Locate every blood parasite and identify its species.
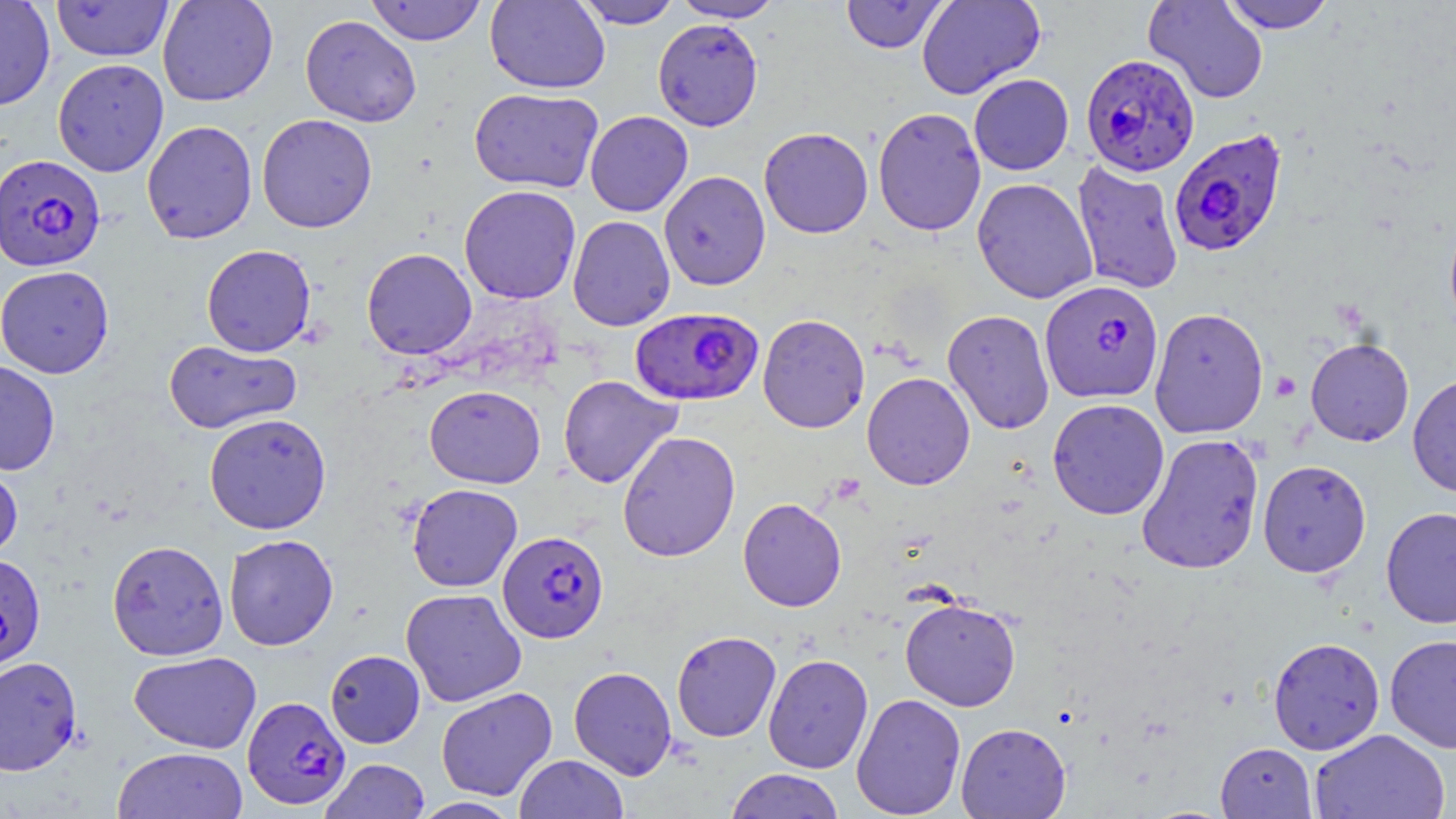
Approximate bounding boxes as [x1, y1, x2, y2] in pixels.
Plasmodium falciparum-infected red blood cells: [1080, 53, 1199, 176], [1168, 127, 1289, 257], [0, 154, 105, 271], [1040, 279, 1164, 404], [630, 306, 763, 407], [497, 530, 608, 643], [0, 553, 46, 671], [242, 695, 351, 810].
No Plasmodium ovale, Plasmodium malariae, Plasmodium vivax, Babesia divergens, or Trypanosoma brucei observed.

Uninfected red blood cell locations: [0, 0, 55, 110], [157, 0, 278, 106], [365, 0, 487, 46], [486, 0, 610, 94], [573, 0, 682, 29], [670, 0, 785, 22], [840, 0, 949, 54], [916, 0, 1045, 99], [1143, 0, 1269, 104], [1220, 0, 1335, 33], [51, 1, 174, 62], [300, 14, 422, 127], [652, 18, 763, 131], [53, 59, 169, 175], [969, 74, 1074, 175], [469, 87, 604, 194], [873, 106, 986, 236], [585, 111, 693, 217], [256, 114, 378, 233], [141, 120, 258, 244], [759, 127, 874, 238], [1071, 160, 1184, 295], [658, 170, 771, 291], [972, 177, 1098, 304], [459, 185, 582, 304], [1443, 208, 1456, 341], [567, 215, 675, 331], [201, 244, 316, 356], [361, 248, 477, 359], [0, 265, 114, 378], [1149, 307, 1269, 439], [942, 309, 1055, 434], [757, 313, 870, 433], [1305, 337, 1414, 446], [163, 339, 302, 434], [0, 360, 61, 476], [862, 371, 975, 490], [1407, 372, 1456, 499], [557, 374, 683, 489], [424, 385, 546, 488], [1047, 398, 1169, 520], [204, 413, 331, 534], [616, 430, 741, 562], [1136, 433, 1265, 575], [0, 459, 23, 565], [1257, 460, 1371, 578], [407, 483, 523, 592], [737, 497, 847, 612], [1380, 507, 1456, 629], [223, 534, 339, 651], [106, 540, 229, 660], [401, 588, 527, 706], [900, 596, 1021, 711], [671, 630, 781, 742], [1385, 633, 1456, 753], [1268, 636, 1385, 754], [325, 649, 425, 748], [128, 650, 262, 754], [763, 654, 873, 773], [0, 655, 83, 776], [568, 665, 677, 780], [435, 686, 558, 801], [851, 693, 966, 818], [956, 722, 1070, 818], [1309, 728, 1451, 819], [1215, 742, 1316, 818], [111, 746, 248, 819], [514, 754, 628, 818], [321, 758, 431, 818], [725, 768, 845, 818], [409, 796, 524, 818]. Platelet locations: [1271, 372, 1300, 400]. Slide-level diagnosis: Plasmodium falciparum. May-Grünwald-Giemsa stain. Captured at 1000x magnification. Image is 1456×819 pixels. Single field of view. Thin blood smear. Light microscopy.